Locate every Plasmodium parasite.
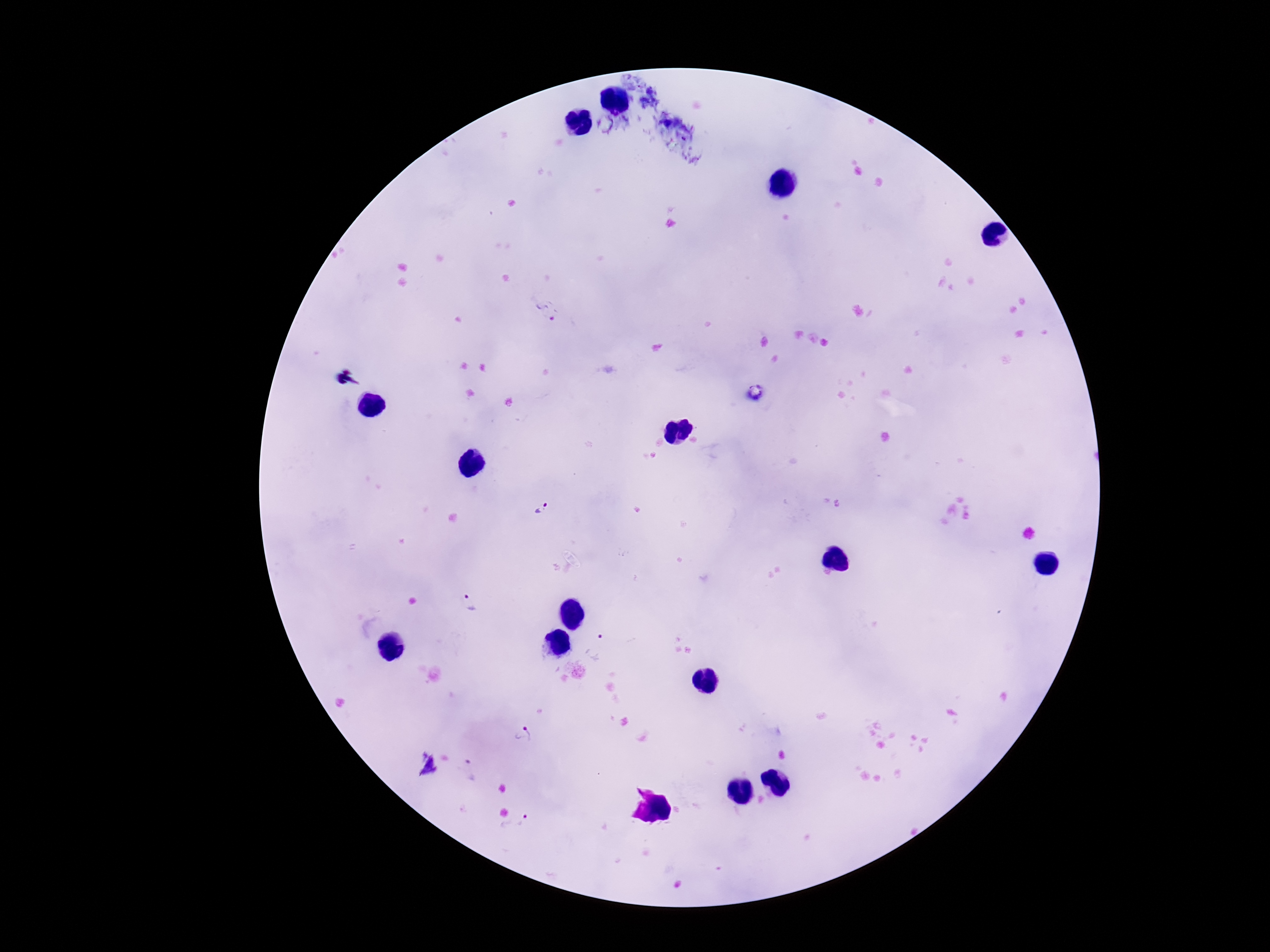

Approximate object centers, in pixels from the top-left corner.
Plasmodium parasites: (x=548, y=310), (x=542, y=509), (x=466, y=601), (x=600, y=639), (x=525, y=732), (x=469, y=771), (x=521, y=828).

{
  "patient_malaria_status": "positive",
  "image_size": "1270×952 pixels",
  "capture": "smartphone camera through the microscope eyepiece",
  "field_of_view": "single",
  "preparation": "thick peripheral-blood smear",
  "stain": "Giemsa",
  "magnification": "100x"
}